Give the position of every Plasmodium falciparum parasite, noting its life-cycle stage.
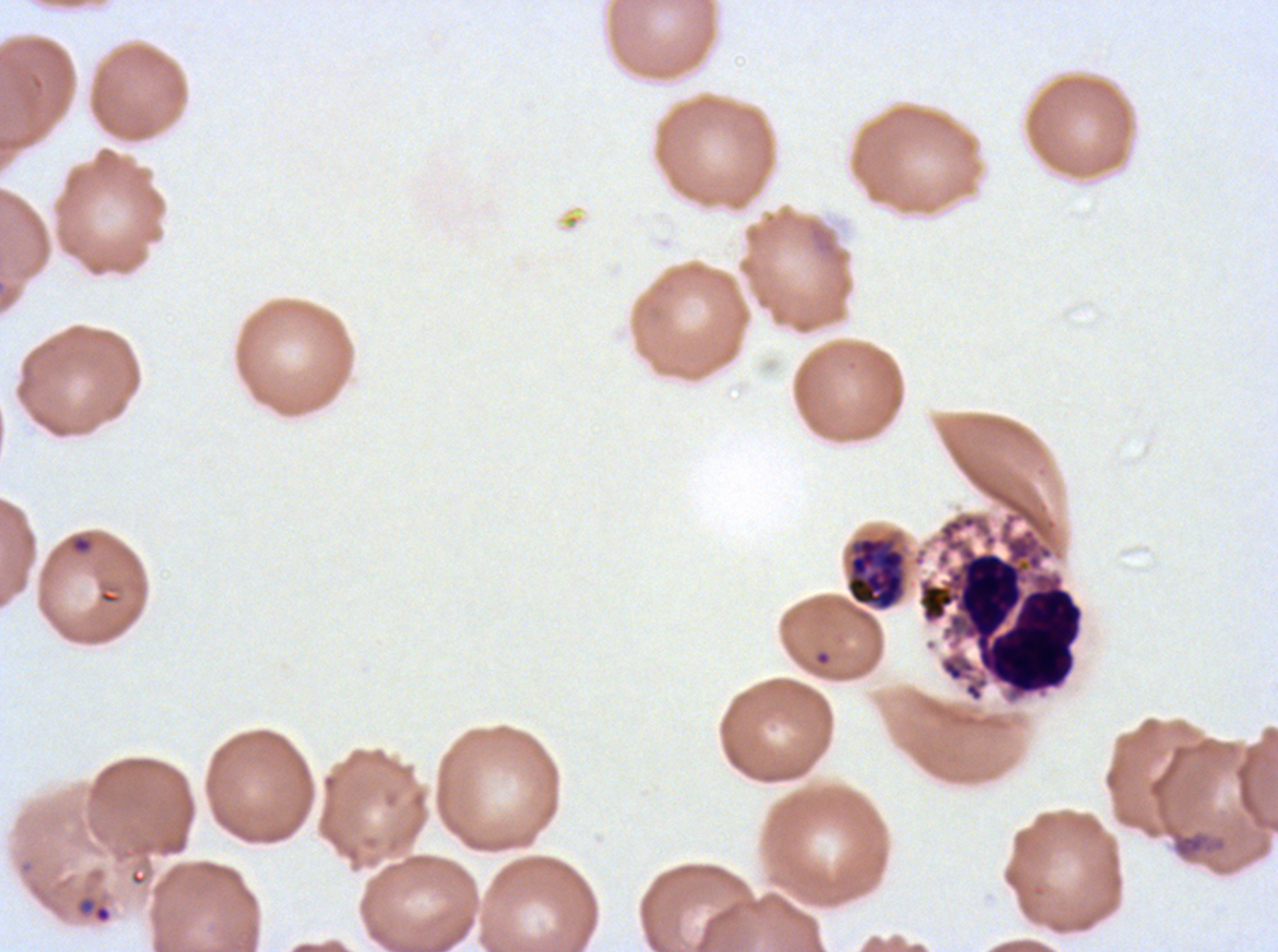

Approximate bounding boxes as (x1, y1, x2, y2) in pixels.
Rings: (69, 533, 94, 555), (75, 895, 113, 925).
Late schizonts: (845, 532, 909, 612).
No late-ring/early-trophozoite forms, mid trophozoites, late trophozoites, early schizonts, segmenters, or gametocytes observed.

Leukocyte locations: (917, 514, 1085, 701). Debris locations: (1171, 830, 1226, 860). Life-cycle stages observed: ring, late schizont. A sub-image separated from a larger composite. Thin blood film. Image is 1278×952 pixels. Plasmodium falciparum from a patient in The Gambia, cultured ex vivo for 24 to 48 hours. Giemsa-stained preparation.